Outline each blood parasite and name the species.
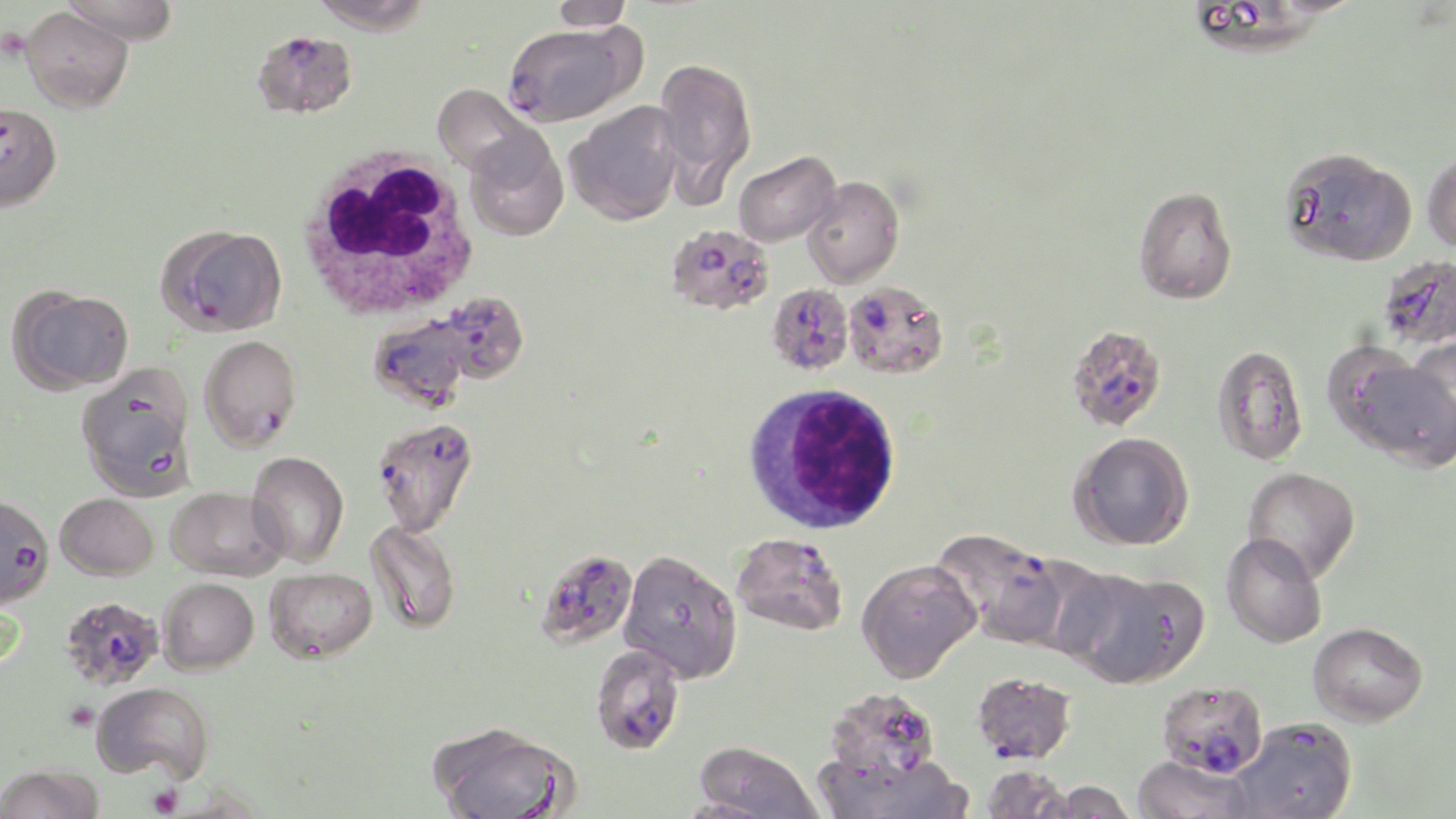
Approximate bounding boxes as named x1/y1/x2/y2 corners in pixels.
Plasmodium falciparum-infected red blood cells (subset): (x1=502, y1=23, x2=637, y2=125), (x1=252, y1=29, x2=359, y2=119), (x1=159, y1=224, x2=287, y2=336), (x1=674, y1=226, x2=778, y2=313), (x1=1377, y1=255, x2=1456, y2=351), (x1=842, y1=281, x2=949, y2=380), (x1=767, y1=282, x2=853, y2=375), (x1=439, y1=291, x2=529, y2=383), (x1=369, y1=314, x2=470, y2=410), (x1=1066, y1=324, x2=1167, y2=431), (x1=200, y1=334, x2=302, y2=452), (x1=370, y1=416, x2=477, y2=536), (x1=0, y1=494, x2=53, y2=608), (x1=933, y1=528, x2=1066, y2=648), (x1=732, y1=532, x2=848, y2=636), (x1=535, y1=548, x2=638, y2=650), (x1=60, y1=596, x2=164, y2=690), (x1=589, y1=644, x2=686, y2=755), (x1=972, y1=671, x2=1077, y2=764), (x1=1156, y1=680, x2=1268, y2=778).
No Plasmodium ovale, Plasmodium malariae, Plasmodium vivax, Babesia divergens, or Trypanosoma brucei observed.

Uninfected red blood cell locations (subset): (x1=62, y1=0, x2=180, y2=45), (x1=309, y1=0, x2=433, y2=35), (x1=550, y1=0, x2=634, y2=31), (x1=1193, y1=0, x2=1326, y2=60), (x1=20, y1=6, x2=133, y2=113), (x1=654, y1=56, x2=757, y2=197), (x1=432, y1=83, x2=535, y2=176), (x1=565, y1=102, x2=683, y2=226), (x1=464, y1=130, x2=569, y2=242), (x1=1279, y1=146, x2=1417, y2=267), (x1=733, y1=149, x2=840, y2=247), (x1=1422, y1=149, x2=1456, y2=254), (x1=801, y1=175, x2=904, y2=287), (x1=1133, y1=185, x2=1238, y2=305), (x1=9, y1=287, x2=133, y2=393), (x1=1395, y1=339, x2=1455, y2=459), (x1=1323, y1=342, x2=1441, y2=459), (x1=1212, y1=344, x2=1309, y2=465), (x1=76, y1=368, x2=198, y2=501), (x1=1069, y1=431, x2=1194, y2=551), (x1=246, y1=450, x2=349, y2=567), (x1=1242, y1=467, x2=1361, y2=583), (x1=166, y1=486, x2=288, y2=581), (x1=56, y1=493, x2=158, y2=580), (x1=364, y1=520, x2=462, y2=634), (x1=1221, y1=533, x2=1327, y2=648), (x1=617, y1=549, x2=743, y2=683), (x1=1004, y1=553, x2=1117, y2=659), (x1=856, y1=558, x2=980, y2=682), (x1=265, y1=567, x2=377, y2=661), (x1=1064, y1=568, x2=1204, y2=690), (x1=158, y1=578, x2=258, y2=674), (x1=1308, y1=621, x2=1428, y2=726), (x1=91, y1=682, x2=214, y2=782), (x1=823, y1=686, x2=941, y2=789), (x1=1229, y1=718, x2=1358, y2=819), (x1=429, y1=720, x2=578, y2=819), (x1=693, y1=741, x2=825, y2=819), (x1=826, y1=752, x2=973, y2=819), (x1=1132, y1=753, x2=1254, y2=819), (x1=0, y1=764, x2=104, y2=819), (x1=980, y1=764, x2=1073, y2=819), (x1=1039, y1=780, x2=1138, y2=818), (x1=672, y1=798, x2=781, y2=819). Platelet locations: (x1=65, y1=700, x2=99, y2=730), (x1=147, y1=784, x2=183, y2=817). White blood cell locations: (x1=295, y1=144, x2=483, y2=323), (x1=742, y1=382, x2=904, y2=535). Slide-level diagnosis: Plasmodium falciparum. Thin blood film. Light microscopy. Image is 1456×819 pixels. Captured at 1000x magnification. Single field of view. May-Grünwald-Giemsa-stained preparation.